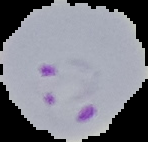
image_type: cell region segmented out of the field of view; surrounding area masked to black
result: malaria parasites detected
preparation: thin blood film
image_size: 148×142 pixels